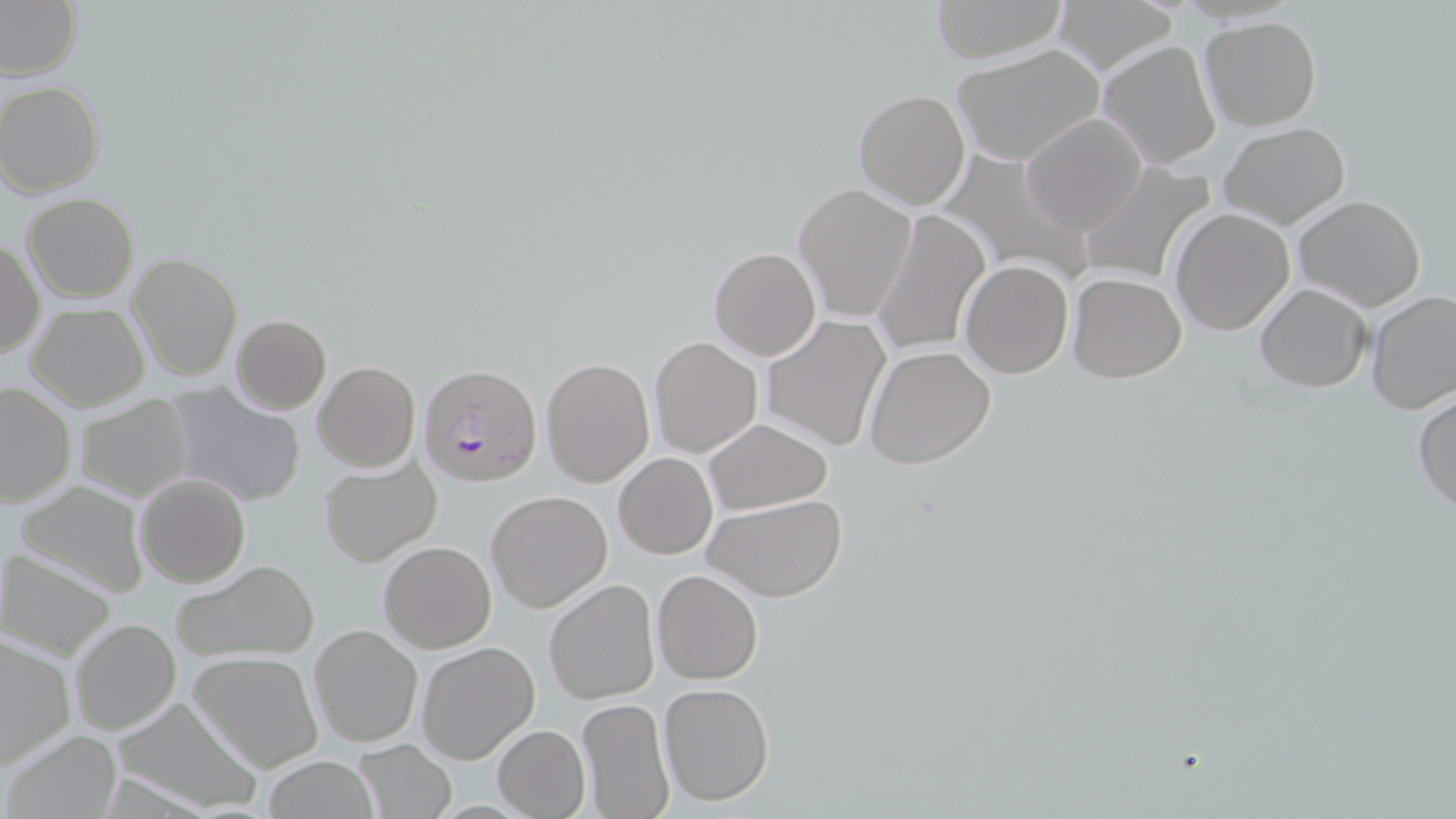

Approximate bounding boxes as (x1, y1, x2, y2) in pixels. Uninfected red blood cell locations: (928, 0, 1069, 61), (1053, 0, 1178, 70), (0, 1, 80, 78), (1200, 17, 1322, 130), (1099, 39, 1221, 170), (952, 43, 1103, 165), (0, 81, 105, 197), (853, 90, 970, 210), (1021, 113, 1147, 237), (1218, 123, 1350, 229), (1081, 159, 1221, 286), (793, 183, 917, 323), (22, 192, 138, 301), (1294, 196, 1425, 311), (1170, 207, 1296, 335), (872, 211, 989, 357), (1, 238, 45, 359), (709, 246, 821, 360), (126, 252, 244, 381), (960, 260, 1073, 378), (1067, 273, 1187, 383), (1255, 282, 1371, 392), (1367, 290, 1455, 415), (27, 301, 149, 410), (231, 315, 330, 413), (760, 316, 890, 451), (649, 336, 761, 457), (863, 344, 997, 469), (541, 356, 654, 487), (314, 361, 421, 472), (0, 381, 76, 508), (162, 382, 306, 508), (1413, 392, 1456, 516), (74, 395, 195, 501), (705, 418, 832, 514), (615, 453, 717, 559), (318, 455, 442, 568), (134, 472, 249, 588), (11, 480, 151, 599), (486, 490, 613, 612), (705, 495, 846, 603), (378, 540, 496, 653), (1, 549, 118, 661), (170, 560, 319, 663), (652, 570, 762, 684), (544, 579, 660, 706), (69, 618, 181, 736), (309, 624, 422, 748), (0, 633, 76, 769), (416, 640, 540, 764), (190, 652, 324, 773), (659, 683, 773, 804), (115, 696, 263, 815), (576, 698, 674, 818), (492, 725, 589, 818), (5, 730, 120, 817), (351, 739, 458, 819), (261, 757, 381, 817). Plasmodium falciparum-infected red blood cell locations: (418, 364, 541, 490). Slide-level diagnosis: Plasmodium falciparum. Light microscopy. Captured at 1000x magnification. Thin blood smear. Image is 1456×819 pixels. May-Grünwald-Giemsa-stained preparation. One field of a larger specimen.